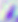
Photomicrograph. Toxoplasma gondii is shown. 400x magnification.